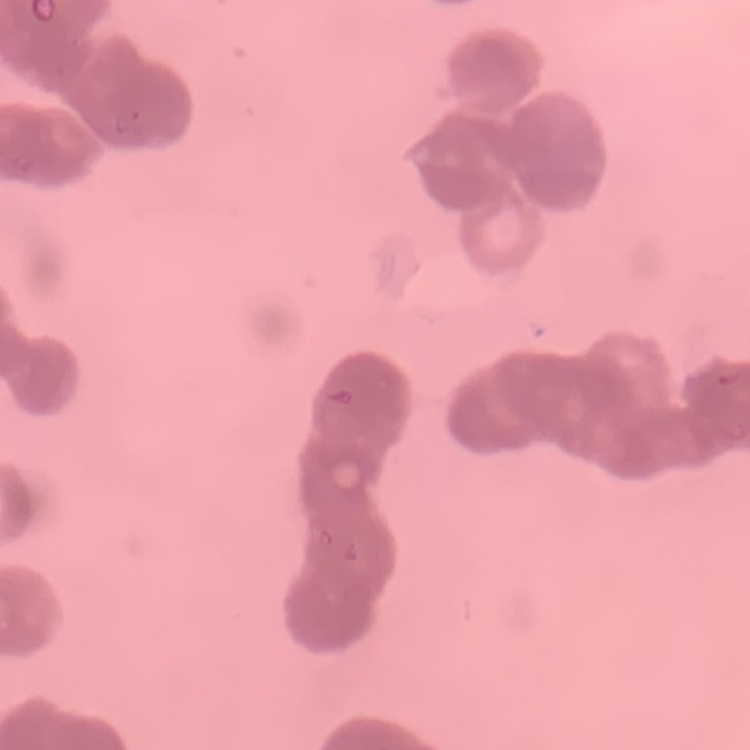

erythrocyte morphology = rouleaux formation
stain = Field's or Giemsa
preparation = thin blood smear
image type = square crop of a larger photomicrograph